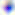

Summary:
  - Modality: micrograph
  - Identification: Toxoplasma gondii
  - Magnification: 400x